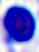

modality = photomicrograph
magnification = 400x
identification = white blood cell